Assess this cell for malaria.
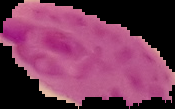
Parasitized.

Summary:
  - Image size: 175×109 pixels
  - Preparation: thin blood smear
  - Image type: cell region segmented out of the field of view; surrounding area masked to black